Classify this cell by malaria status.
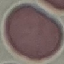

It is uninfected.

capture = smartphone through the microscope eyepiece
image type = automatically extracted cell patch, resized to 64 × 64 pixels
preparation = thin blood film
stain = Giemsa